Assess this cell for malaria.
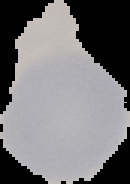
Uninfected.

image size = 130×184 pixels
image type = segmented cell region with the area outside set to black
preparation = thin blood smear